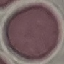
Summary:
  - Result: no malaria parasites detected
  - Preparation: thin smear
  - Capture: smartphone through the microscope eyepiece
  - Stain: Giemsa
  - Image type: automatically extracted cell patch, resized to 64 × 64 pixels